Describe the morphology of the erythrocytes.
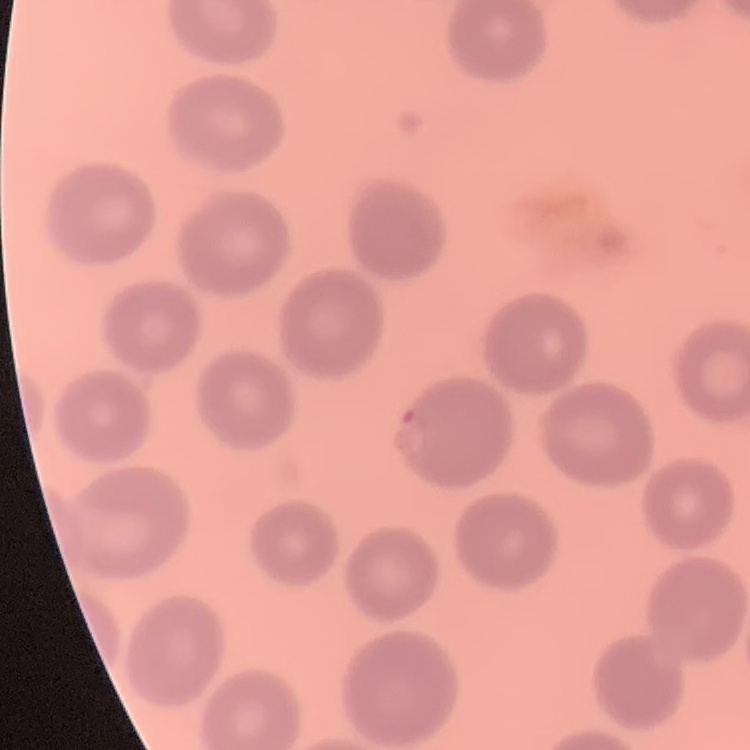
No rouleaux formation.

preparation = thin peripheral smear
stain = Field's or Giemsa
image type = one tile cut from a larger photomicrograph